Locate and identify every blood parasite.
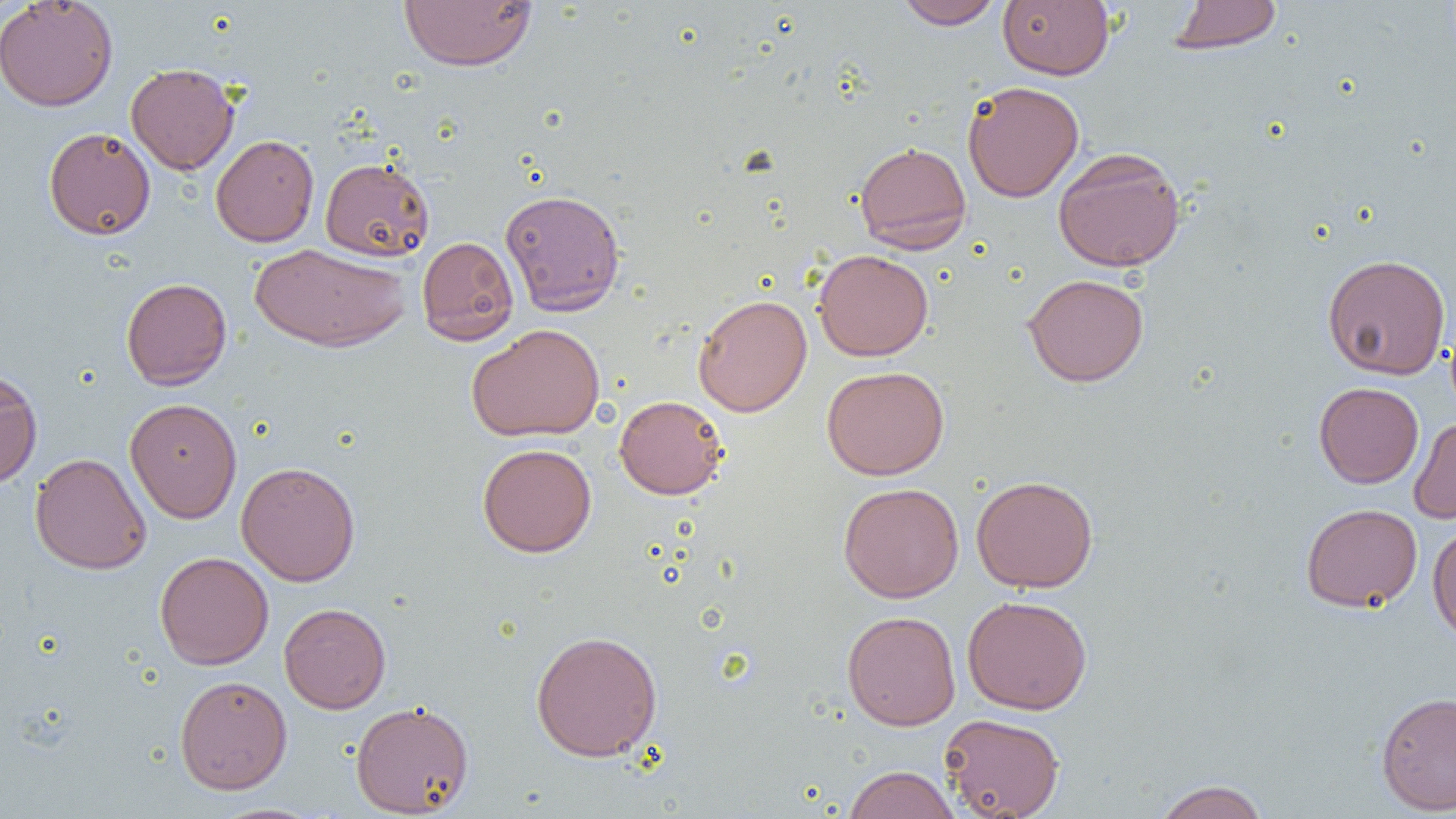

No blood parasites observed.

slide-level diagnosis = negative for blood parasites
preparation = thin blood film
magnification = 1000x
modality = optical microscopy
uninfected red blood cell locations = approximate bounding boxes as (x1,y1)-(x2,y2) corner pairs in pixels: (0,0)-(118,111), (400,0)-(538,71), (894,0)-(1004,29), (998,0)-(1114,80), (1167,1)-(1282,54), (126,63)-(239,174), (963,81)-(1084,202), (44,127)-(156,240), (210,134)-(319,247), (854,142)-(972,253), (1052,147)-(1186,272), (320,157)-(434,262), (500,188)-(625,316), (417,236)-(519,345), (249,243)-(410,352), (813,249)-(933,361), (1322,254)-(1451,380), (1022,273)-(1149,387), (121,277)-(232,390), (693,294)-(812,416), (466,323)-(605,442), (822,366)-(949,480), (0,368)-(42,489), (1314,382)-(1424,488), (614,395)-(727,499), (125,398)-(242,523), (1408,416)-(1456,524), (477,442)-(596,557), (30,453)-(151,574), (236,460)-(361,586), (971,474)-(1099,592), (838,482)-(964,602), (1300,503)-(1423,612), (1427,523)-(1456,645), (155,551)-(274,670), (962,595)-(1092,715), (279,602)-(391,714), (842,610)-(960,730), (530,629)-(663,762), (174,674)-(292,794), (1375,691)-(1456,815), (350,699)-(474,817), (939,713)-(1065,819), (842,765)-(960,819), (1153,779)-(1271,819)
image size = 1456×819 pixels
field of view = single